Name the cell type shown.
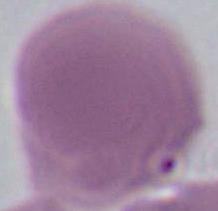
This is an erythrocyte.

Captured at 1000x magnification. Photomicrograph.